State which parasite is depicted.
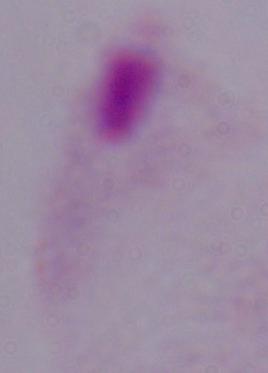
This is a trichomonad.

magnification = 1000x
modality = photomicrograph